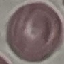

Summary:
  - Result: negative for malaria parasites
  - Image type: cell patch, automatically extracted from a larger field of view and resized to 64 × 64 pixels
  - Stain: Giemsa
  - Preparation: thin smear
  - Capture: smartphone camera at the microscope eyepiece